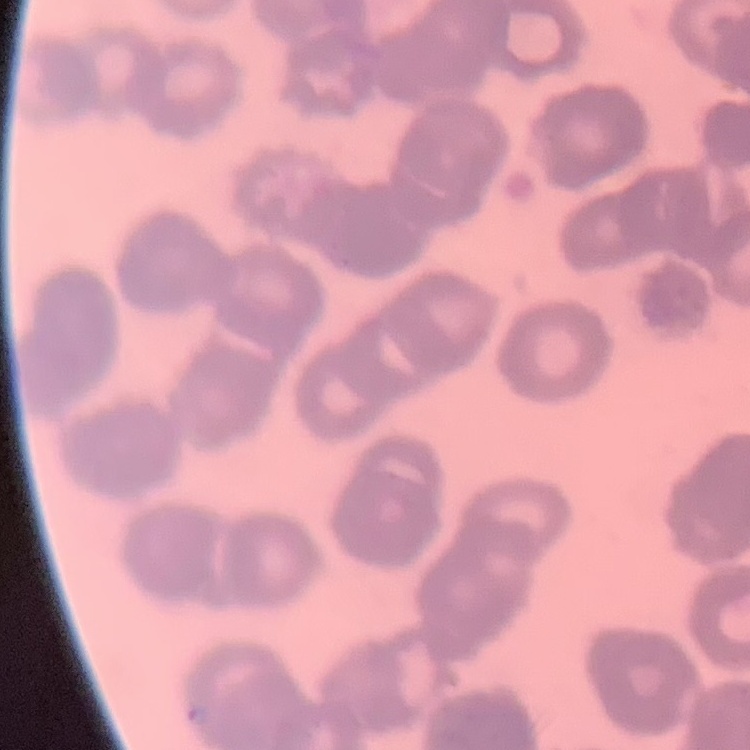
The red blood cells exhibit rouleaux formation. Stained with either Field's or Giemsa. Thin blood smear. One tile cut from a larger photomicrograph.